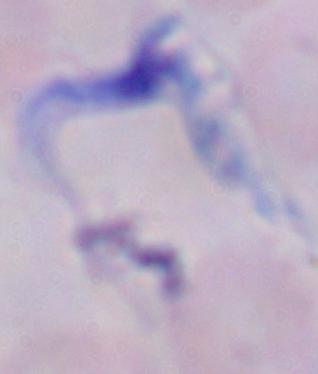
Summary:
  - Magnification: 1000x
  - Identification: trypanosome
  - Modality: photomicrograph